Outline each Plasmodium vivax-infected red blood cell.
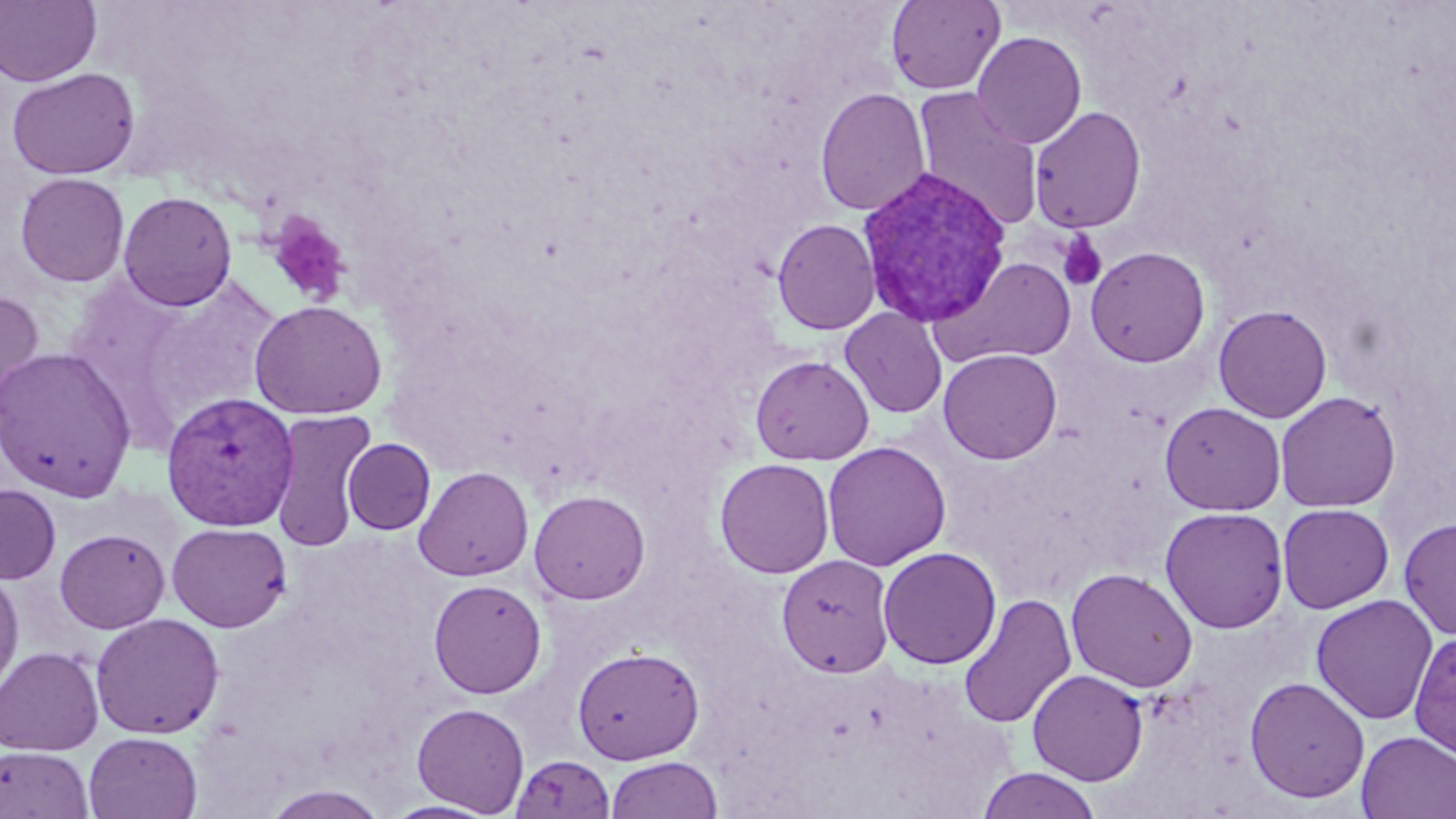
Approximate bounding boxes as named x1/y1/x2/y2 corners in pixels.
Plasmodium vivax-infected red blood cells: (x1=856, y1=165, x2=1013, y2=328), (x1=161, y1=392, x2=300, y2=531).

Summary:
  - Uninfected red blood cell locations: (x1=0, y1=0, x2=101, y2=87), (x1=886, y1=0, x2=1005, y2=94), (x1=972, y1=31, x2=1087, y2=149), (x1=6, y1=68, x2=140, y2=180), (x1=912, y1=87, x2=1044, y2=232), (x1=815, y1=88, x2=930, y2=217), (x1=1029, y1=106, x2=1146, y2=233), (x1=15, y1=172, x2=130, y2=287), (x1=118, y1=191, x2=238, y2=311), (x1=772, y1=218, x2=880, y2=335), (x1=1085, y1=246, x2=1210, y2=367), (x1=938, y1=257, x2=1079, y2=367), (x1=0, y1=288, x2=45, y2=423), (x1=249, y1=300, x2=387, y2=419), (x1=1213, y1=304, x2=1332, y2=423), (x1=840, y1=307, x2=948, y2=419), (x1=0, y1=346, x2=136, y2=501), (x1=938, y1=348, x2=1062, y2=464), (x1=751, y1=355, x2=874, y2=465), (x1=1275, y1=391, x2=1401, y2=512), (x1=1159, y1=401, x2=1286, y2=515), (x1=268, y1=408, x2=378, y2=550), (x1=342, y1=438, x2=436, y2=534), (x1=822, y1=441, x2=951, y2=571), (x1=714, y1=458, x2=834, y2=579), (x1=414, y1=466, x2=534, y2=581), (x1=1, y1=484, x2=60, y2=584), (x1=529, y1=490, x2=650, y2=604), (x1=1277, y1=503, x2=1394, y2=613), (x1=1160, y1=506, x2=1289, y2=633), (x1=1398, y1=516, x2=1456, y2=640), (x1=167, y1=522, x2=292, y2=632), (x1=54, y1=528, x2=170, y2=633), (x1=878, y1=546, x2=1002, y2=669), (x1=777, y1=554, x2=895, y2=677), (x1=0, y1=567, x2=24, y2=696), (x1=1065, y1=568, x2=1198, y2=693), (x1=428, y1=579, x2=547, y2=699), (x1=958, y1=593, x2=1077, y2=730), (x1=1311, y1=595, x2=1438, y2=725), (x1=90, y1=613, x2=225, y2=739), (x1=1409, y1=630, x2=1456, y2=761), (x1=0, y1=646, x2=104, y2=756), (x1=573, y1=646, x2=704, y2=764), (x1=1028, y1=669, x2=1148, y2=786), (x1=1244, y1=676, x2=1370, y2=803), (x1=412, y1=703, x2=529, y2=815), (x1=84, y1=731, x2=202, y2=819), (x1=1356, y1=731, x2=1456, y2=818), (x1=0, y1=745, x2=94, y2=818), (x1=510, y1=754, x2=616, y2=819), (x1=604, y1=756, x2=723, y2=819), (x1=976, y1=768, x2=1103, y2=819), (x1=261, y1=784, x2=389, y2=819), (x1=381, y1=800, x2=501, y2=818)
  - Platelet locations: (x1=268, y1=213, x2=350, y2=305), (x1=1057, y1=232, x2=1108, y2=292)
  - Slide-level diagnosis: Plasmodium vivax
  - Field of view: one of a larger specimen
  - Modality: light microscopy
  - Magnification: 1000x
  - Image size: 1456×819 pixels
  - Preparation: thin blood film
  - Stain: May-Grünwald-Giemsa